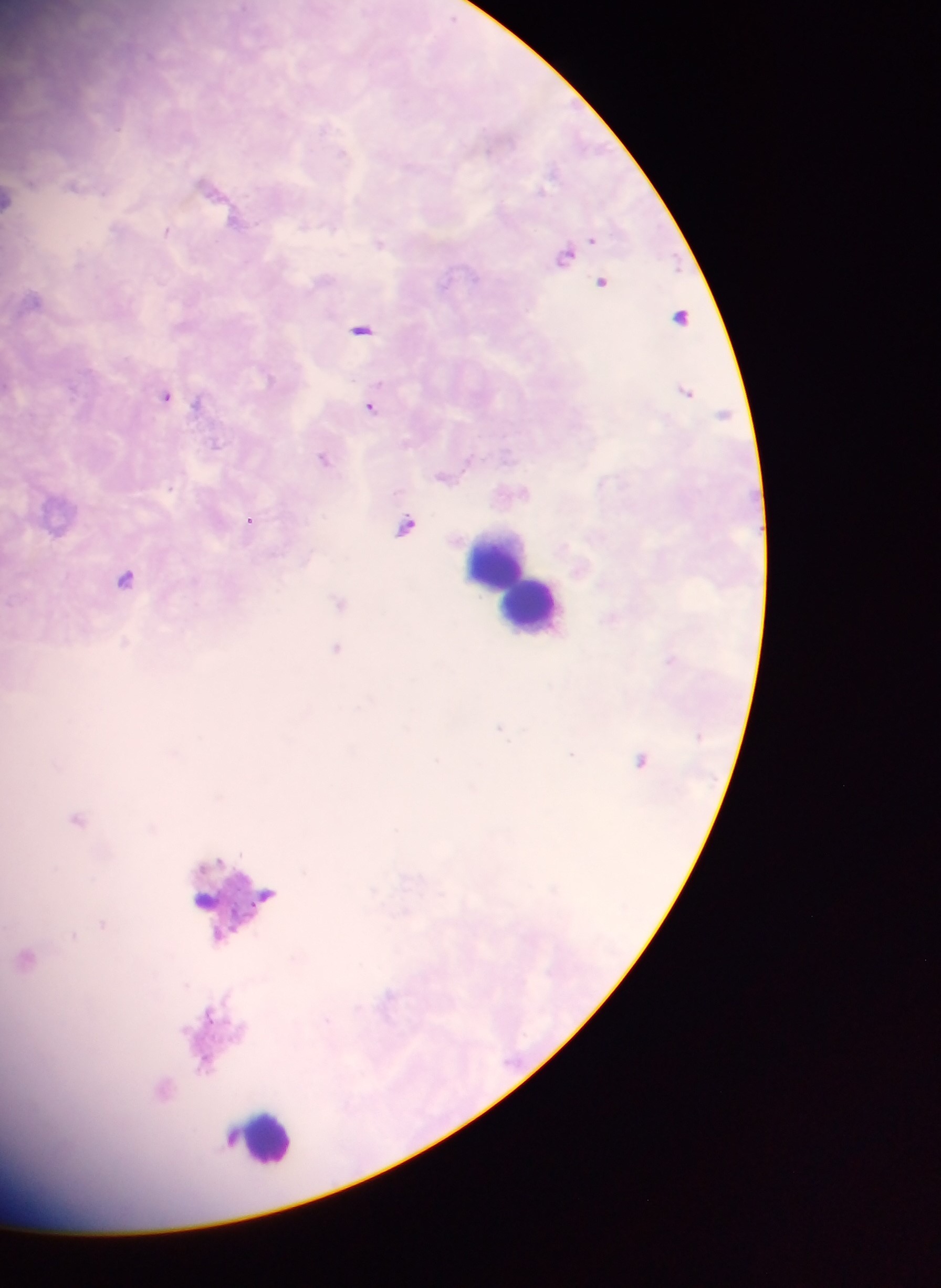

Approximate centers as x y in pixels. Plasmodium parasite locations: 74 185; 210 186; 11 199; 168 229; 379 243; 565 255; 601 280; 681 316; 361 329; 684 391; 167 395; 371 406; 325 458; 443 476; 250 520; 407 525; 125 577; 340 602; 336 649; 640 759; 77 819; 25 957; 164 1089. Leukocyte locations: 504 566; 531 601; 237 897; 206 899; 261 1138. Sample from Ghana. One field of view. Image is 941×1288 pixels. Thick blood smear. Mobile-phone photograph taken through the microscope.